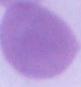
magnification = 1000x
modality = photomicrograph
identification = erythrocyte